Report the malaria status of this cell.
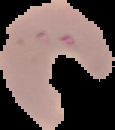

It is parasitized.

image size = 115×130 pixels
image type = cell region segmented out of the field of view; surrounding area masked to black
preparation = thin blood smear